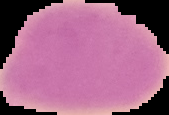

malaria status = uninfected
preparation = thin blood film
image type = cell region segmented out of the field of view; surrounding area masked to black
image size = 169×115 pixels